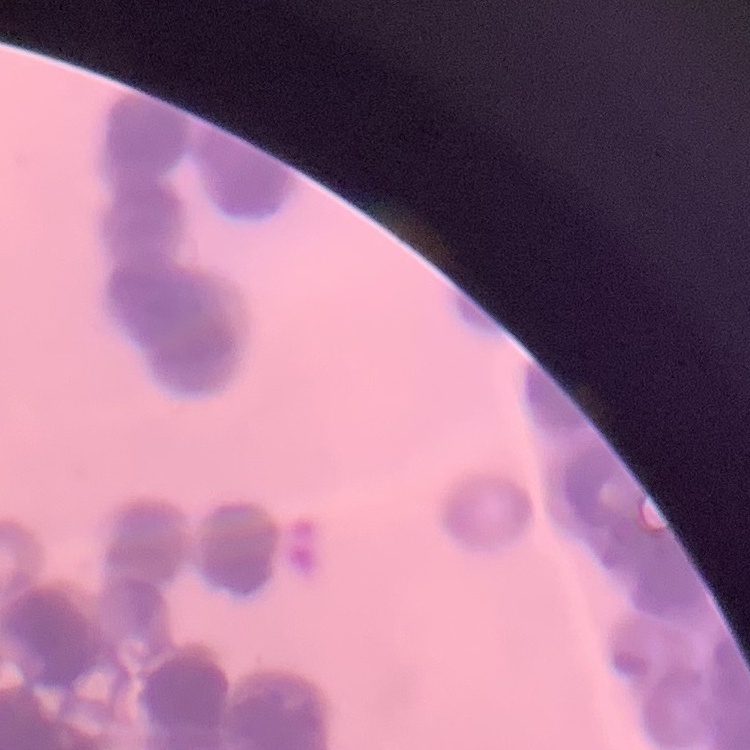

{
  "erythrocyte_morphology": "rouleaux formation",
  "stain": "Field's or Giemsa",
  "preparation": "thin blood film",
  "image_type": "square crop of a larger photomicrograph"
}